Report the malaria status of this cell.
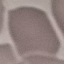
It is uninfected.

stain = Giemsa
capture = smartphone camera at the microscope eyepiece
preparation = thin blood film
image type = cell patch, automatically extracted from a larger field of view and resized to 64 × 64 pixels